State the blood parasite species.
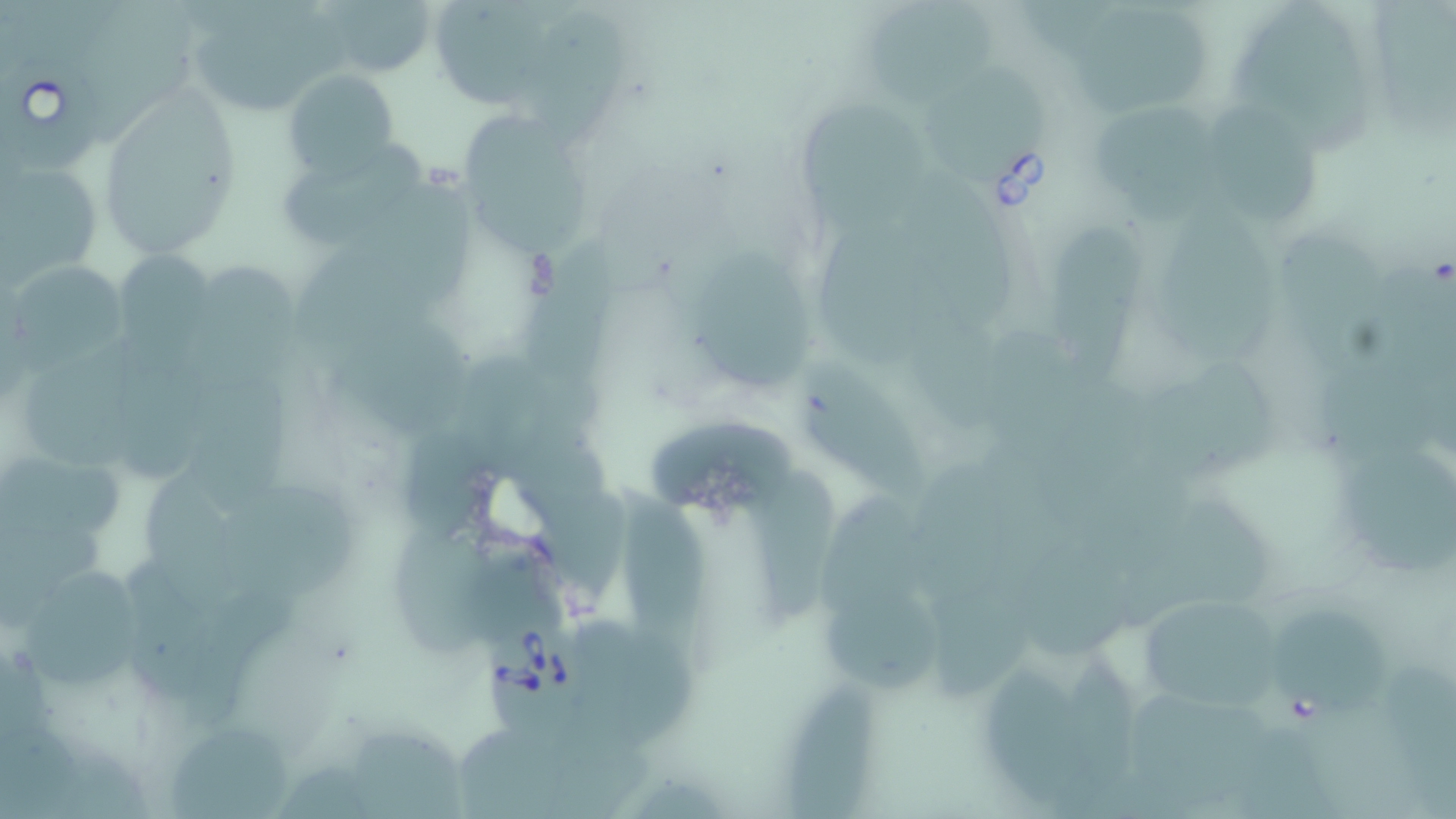

Babesia divergens.

Approximate bounding boxes as named x1/y1/x2/y2 corners in pixels. Uninfected red blood cell locations: (x1=1382, y1=0, x2=1456, y2=129), (x1=322, y1=1, x2=435, y2=77), (x1=1245, y1=3, x2=1378, y2=150), (x1=872, y1=4, x2=998, y2=108), (x1=1071, y1=6, x2=1208, y2=113), (x1=184, y1=14, x2=351, y2=115), (x1=522, y1=14, x2=635, y2=140), (x1=923, y1=67, x2=1040, y2=183), (x1=285, y1=69, x2=399, y2=178), (x1=97, y1=87, x2=243, y2=257), (x1=792, y1=93, x2=930, y2=229), (x1=1211, y1=100, x2=1322, y2=230), (x1=1094, y1=106, x2=1239, y2=233), (x1=458, y1=115, x2=595, y2=266), (x1=280, y1=142, x2=423, y2=244), (x1=1, y1=156, x2=103, y2=285), (x1=911, y1=176, x2=1025, y2=332), (x1=366, y1=179, x2=473, y2=300), (x1=1158, y1=200, x2=1278, y2=371), (x1=814, y1=219, x2=960, y2=370), (x1=1049, y1=220, x2=1143, y2=368), (x1=1278, y1=230, x2=1393, y2=376), (x1=523, y1=236, x2=624, y2=383), (x1=293, y1=242, x2=448, y2=360), (x1=691, y1=242, x2=818, y2=388), (x1=115, y1=252, x2=219, y2=367), (x1=18, y1=258, x2=128, y2=379), (x1=179, y1=266, x2=298, y2=393), (x1=906, y1=314, x2=1005, y2=437), (x1=327, y1=316, x2=472, y2=441), (x1=25, y1=338, x2=145, y2=469), (x1=121, y1=351, x2=215, y2=485), (x1=455, y1=356, x2=606, y2=472), (x1=1150, y1=361, x2=1277, y2=491), (x1=792, y1=362, x2=934, y2=502), (x1=186, y1=375, x2=297, y2=512), (x1=647, y1=419, x2=799, y2=515), (x1=1336, y1=438, x2=1453, y2=568), (x1=2, y1=452, x2=134, y2=541), (x1=757, y1=466, x2=842, y2=625), (x1=141, y1=467, x2=247, y2=615), (x1=216, y1=479, x2=365, y2=606), (x1=617, y1=487, x2=710, y2=664), (x1=819, y1=491, x2=921, y2=620), (x1=388, y1=520, x2=503, y2=659), (x1=1024, y1=543, x2=1136, y2=663), (x1=13, y1=558, x2=148, y2=693), (x1=121, y1=560, x2=217, y2=695), (x1=826, y1=587, x2=948, y2=693), (x1=1141, y1=592, x2=1284, y2=719), (x1=1276, y1=607, x2=1390, y2=713), (x1=576, y1=617, x2=699, y2=748), (x1=1070, y1=651, x2=1147, y2=782), (x1=983, y1=654, x2=1099, y2=808), (x1=789, y1=671, x2=879, y2=819), (x1=347, y1=723, x2=470, y2=819), (x1=168, y1=725, x2=293, y2=819). Babesia divergens-infected red blood cell locations: (x1=1, y1=56, x2=106, y2=178), (x1=482, y1=617, x2=594, y2=735). Optical microscopy. Image is 1456×819 pixels. Thin blood film. May-Grünwald-Giemsa-stained preparation. 1000x magnification. Single field of view.